Identify the cell.
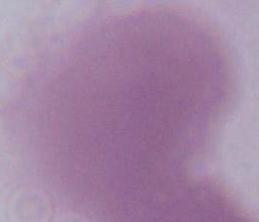
An erythrocyte.

Summary:
  - Magnification: 1000x
  - Modality: photomicrograph